Name the parasite shown.
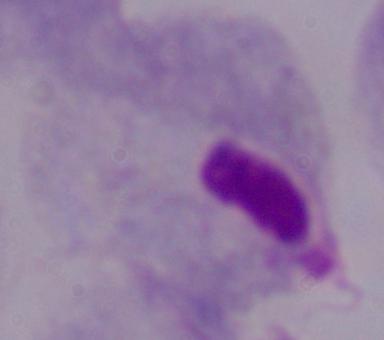

A trichomonad.

magnification = 1000x
modality = photomicrograph